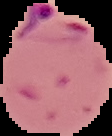

Result: Plasmodium parasites identified. Segmented cell region on a black background. From a thin blood smear. Image is 112×136 pixels.